Give the position of every leukocyte visible.
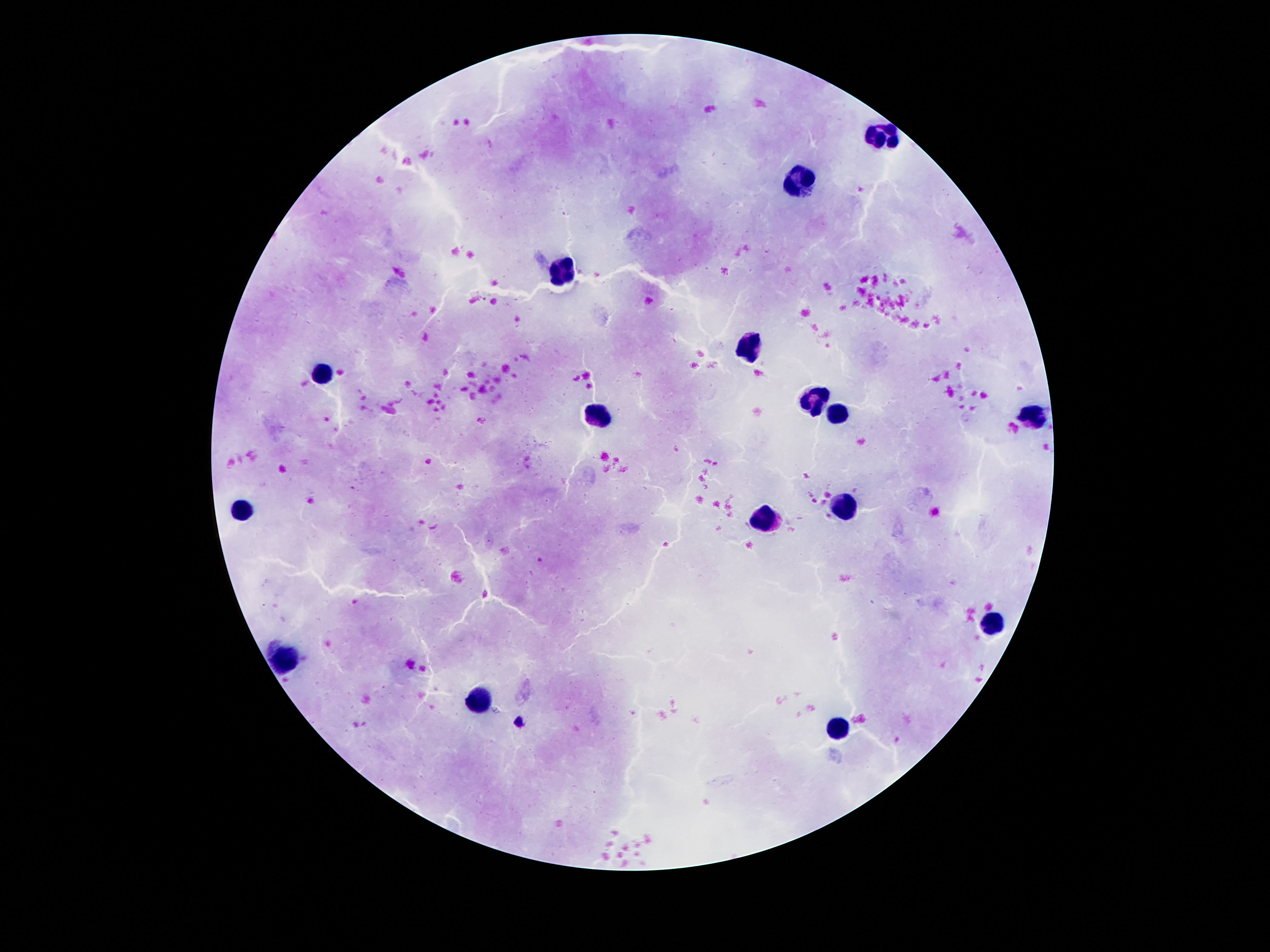

Approximate centers as (x, y) in pixels.
Leukocytes: (884, 139), (801, 183), (564, 271), (747, 351), (325, 376), (815, 396), (834, 412), (595, 415), (1029, 416), (852, 505), (244, 511), (765, 518), (993, 623), (286, 661), (482, 698), (836, 730).

{
  "preparation": "thick blood film",
  "patient_malaria_status": "not infected",
  "magnification": "100x",
  "field_of_view": "one from this slide",
  "capture": "smartphone camera through the microscope eyepiece",
  "stain": "Giemsa",
  "image_size": "1270×952 pixels"
}